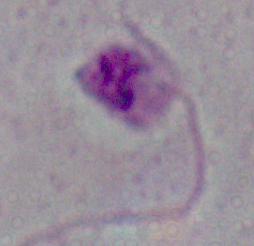
{
  "magnification": "1000x",
  "identification": "Leishmania",
  "modality": "micrograph"
}